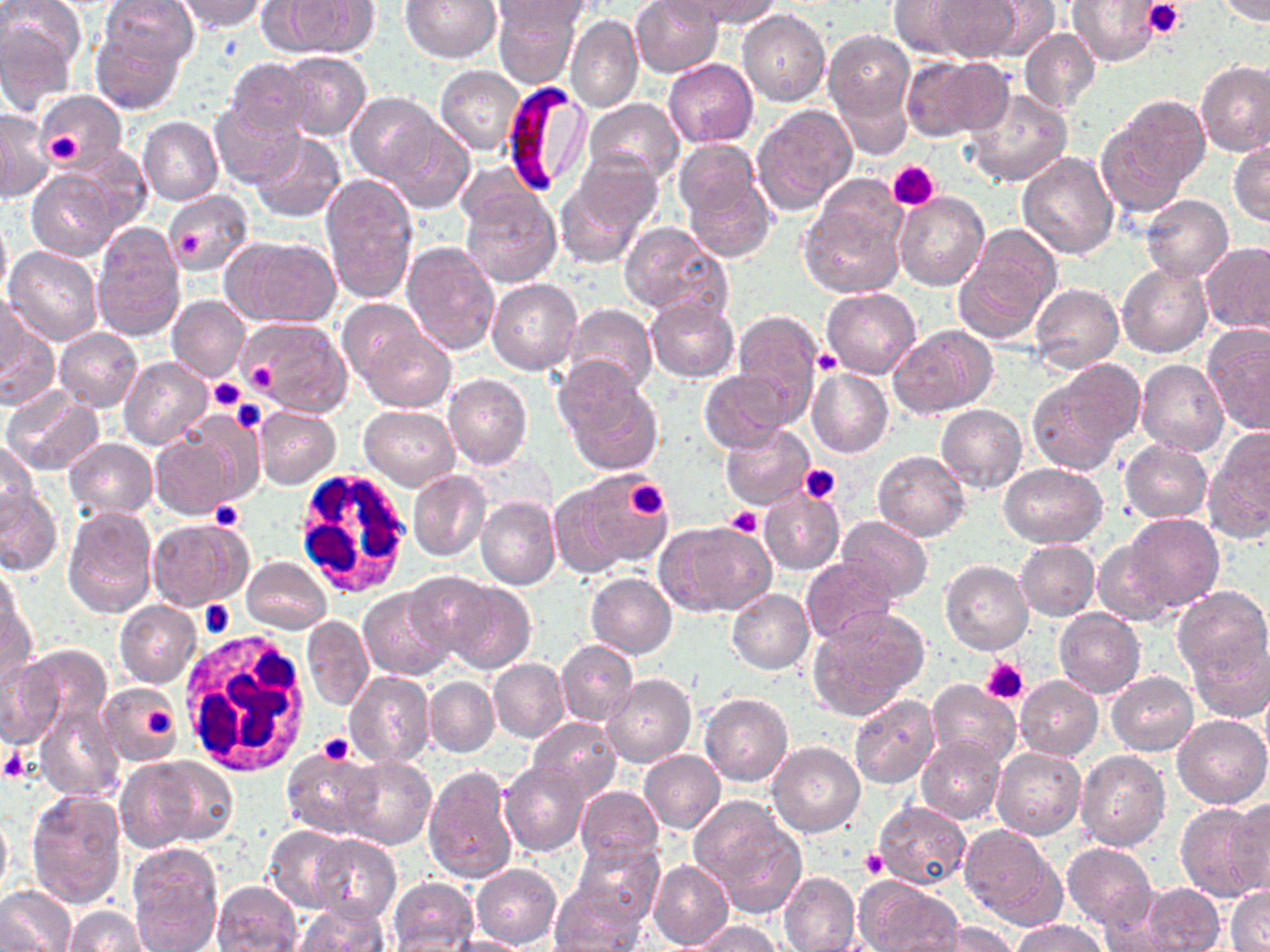 Approximate bounding boxes as (x1, y1, x2, y2) in pixels. Uninfected red blood cell locations: (101, 0, 197, 72), (178, 0, 266, 32), (399, 0, 501, 63), (494, 0, 581, 89), (630, 0, 723, 77), (678, 0, 785, 30), (929, 0, 1025, 62), (973, 0, 1060, 58), (1066, 0, 1163, 66), (1214, 0, 1270, 24), (275, 1, 380, 58), (491, 1, 596, 32), (888, 1, 982, 59), (737, 9, 831, 106), (567, 14, 644, 113), (0, 21, 77, 113), (90, 24, 187, 115), (824, 27, 915, 133), (1020, 28, 1101, 113), (278, 52, 372, 141), (907, 56, 1011, 140), (226, 58, 314, 138), (663, 58, 757, 147), (1196, 59, 1270, 156), (435, 65, 527, 153), (832, 73, 915, 164), (963, 87, 1073, 188), (37, 90, 126, 175), (346, 92, 442, 184), (1099, 96, 1209, 208), (585, 98, 685, 184), (210, 102, 302, 186), (750, 104, 858, 215), (0, 109, 50, 201), (385, 115, 475, 213), (139, 116, 223, 206), (249, 134, 347, 222), (674, 141, 765, 226), (1228, 142, 1270, 226), (1017, 151, 1120, 260), (556, 162, 662, 265), (681, 166, 778, 261), (27, 168, 123, 260), (321, 174, 418, 304), (459, 183, 562, 287), (163, 191, 253, 276), (797, 192, 907, 301), (895, 192, 990, 292), (1138, 195, 1233, 282), (911, 201, 1022, 325), (0, 213, 10, 305), (619, 220, 731, 317), (92, 223, 185, 341), (954, 224, 1062, 344), (221, 235, 340, 328), (402, 241, 500, 355), (1201, 242, 1270, 336), (5, 245, 103, 345), (1117, 262, 1211, 359), (486, 279, 582, 375), (1029, 283, 1123, 374), (822, 288, 921, 378), (1, 293, 26, 388), (167, 295, 252, 383), (645, 298, 738, 381), (338, 301, 429, 385), (0, 302, 57, 407), (562, 304, 658, 394), (731, 310, 824, 421), (238, 316, 355, 420), (890, 324, 998, 417), (1203, 325, 1270, 436), (56, 328, 143, 411), (355, 331, 456, 412), (119, 357, 211, 448), (1027, 360, 1143, 474), (1137, 360, 1229, 457), (554, 361, 662, 475), (807, 368, 893, 460), (697, 369, 794, 450), (443, 374, 532, 469), (0, 389, 104, 475), (935, 404, 1027, 493), (359, 405, 461, 489), (254, 407, 340, 489), (176, 412, 263, 505), (720, 425, 813, 510), (1204, 430, 1270, 543), (150, 431, 240, 520), (64, 439, 157, 519), (1118, 439, 1213, 523), (1, 441, 41, 525), (873, 450, 969, 541), (1000, 463, 1107, 547), (407, 470, 490, 562), (577, 472, 675, 569), (546, 480, 640, 578), (0, 483, 62, 577), (759, 491, 845, 573), (476, 496, 561, 592), (62, 507, 158, 618), (1121, 515, 1225, 613), (838, 517, 933, 602), (147, 518, 251, 611), (654, 521, 775, 617), (1091, 538, 1179, 625), (1014, 541, 1100, 620), (243, 557, 332, 634), (801, 558, 896, 645), (940, 559, 1034, 655), (1, 563, 25, 654), (403, 572, 499, 662), (585, 573, 676, 659), (434, 579, 536, 674), (1173, 585, 1270, 682), (359, 586, 455, 680), (727, 589, 814, 674), (0, 598, 36, 691), (115, 601, 202, 688), (807, 608, 930, 720), (1054, 608, 1146, 699), (301, 615, 373, 711), (1186, 630, 1270, 721), (556, 641, 639, 728), (16, 645, 112, 741), (0, 652, 67, 749), (488, 659, 570, 743), (1106, 671, 1198, 755), (346, 672, 435, 767), (604, 673, 695, 766), (1015, 676, 1103, 760), (426, 677, 499, 756), (926, 679, 1020, 770), (100, 683, 182, 767), (700, 693, 793, 786), (848, 695, 939, 789), (36, 701, 124, 802), (1173, 715, 1270, 809), (528, 718, 622, 801), (917, 735, 1006, 825), (767, 741, 865, 837), (992, 747, 1086, 841), (281, 749, 382, 837), (1076, 750, 1170, 851), (640, 751, 725, 833), (122, 754, 237, 849), (341, 755, 435, 850), (499, 758, 590, 856), (422, 765, 520, 886), (576, 785, 663, 862), (25, 789, 126, 910), (1224, 797, 1270, 896), (691, 800, 805, 918), (873, 800, 972, 890), (1174, 801, 1270, 902), (0, 810, 12, 901), (960, 825, 1067, 931), (263, 826, 358, 913), (308, 835, 400, 924), (570, 839, 664, 927), (1061, 843, 1157, 932), (126, 845, 223, 950), (649, 859, 733, 950), (471, 864, 561, 950), (779, 871, 860, 952), (388, 876, 479, 952), (854, 877, 961, 952), (213, 881, 301, 951), (549, 882, 647, 950), (1134, 883, 1226, 951), (1227, 885, 1270, 952), (0, 887, 75, 952), (292, 902, 387, 952), (66, 906, 147, 952), (1009, 919, 1107, 951), (688, 920, 779, 952), (924, 923, 1022, 952), (441, 934, 530, 952). Platelet locations: (1143, 0, 1186, 40), (43, 131, 83, 164), (889, 161, 940, 211), (180, 232, 206, 260), (814, 352, 842, 375), (245, 359, 280, 391), (208, 377, 244, 413), (230, 399, 268, 433), (800, 463, 840, 502), (623, 479, 670, 520), (210, 501, 245, 533), (725, 506, 764, 536), (200, 599, 235, 637), (982, 658, 1028, 704), (146, 708, 176, 739), (317, 732, 355, 765), (0, 747, 32, 784), (861, 849, 888, 879). White blood cell locations: (291, 470, 414, 599), (179, 632, 313, 776). Plasmodium falciparum-infected red blood cell locations: (504, 86, 593, 196). Slide-level diagnosis: Plasmodium falciparum. Light microscopy. 1000x magnification. Image is 1270×952 pixels. Single field of view. Thin blood film. May-Grünwald-Giemsa stain.